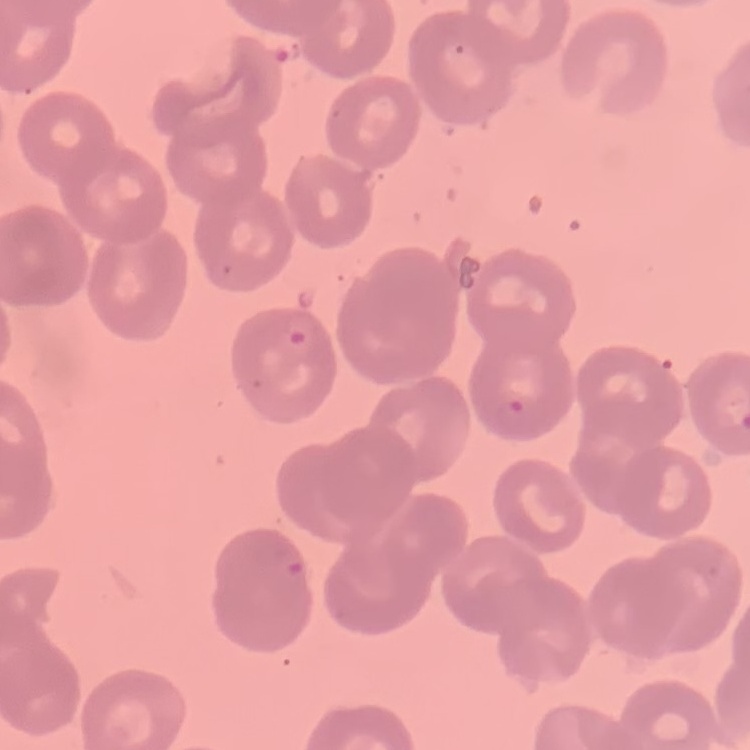

{
  "red_blood_cell_morphology": "no rouleaux formation",
  "stain": "Field's or Giemsa",
  "preparation": "thin blood film",
  "image_type": "one tile cut from a larger photomicrograph"
}